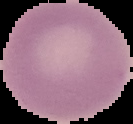
Cell region segmented out of the field of view; the surrounding area is masked to black. From a thin blood film. Result: no Plasmodium parasites detected. Image is 133×124 pixels.